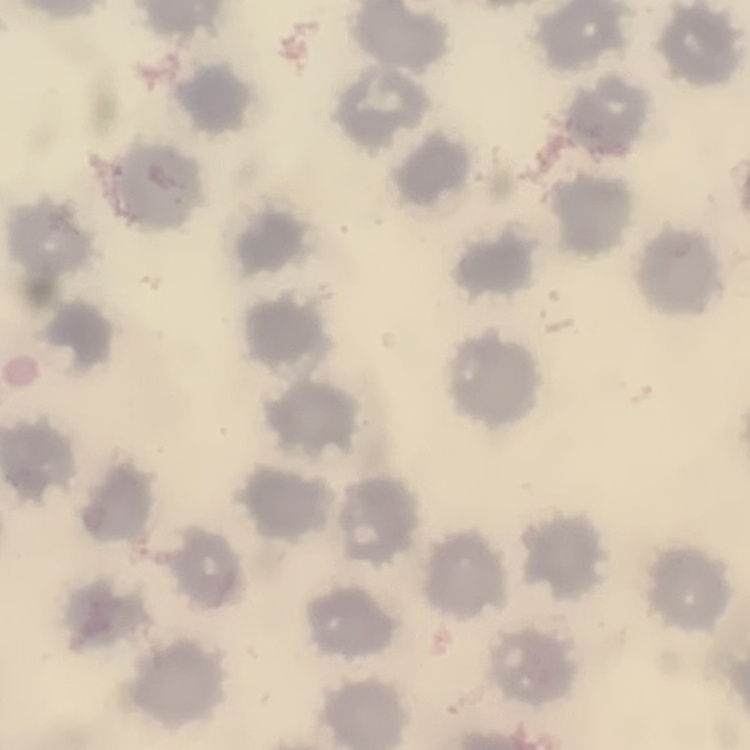

red blood cell morphology = no rouleaux formation
stain = Field's or Giemsa
preparation = thin blood film
image type = one tile cut from a larger photomicrograph